Outline each blood parasite and name the species.
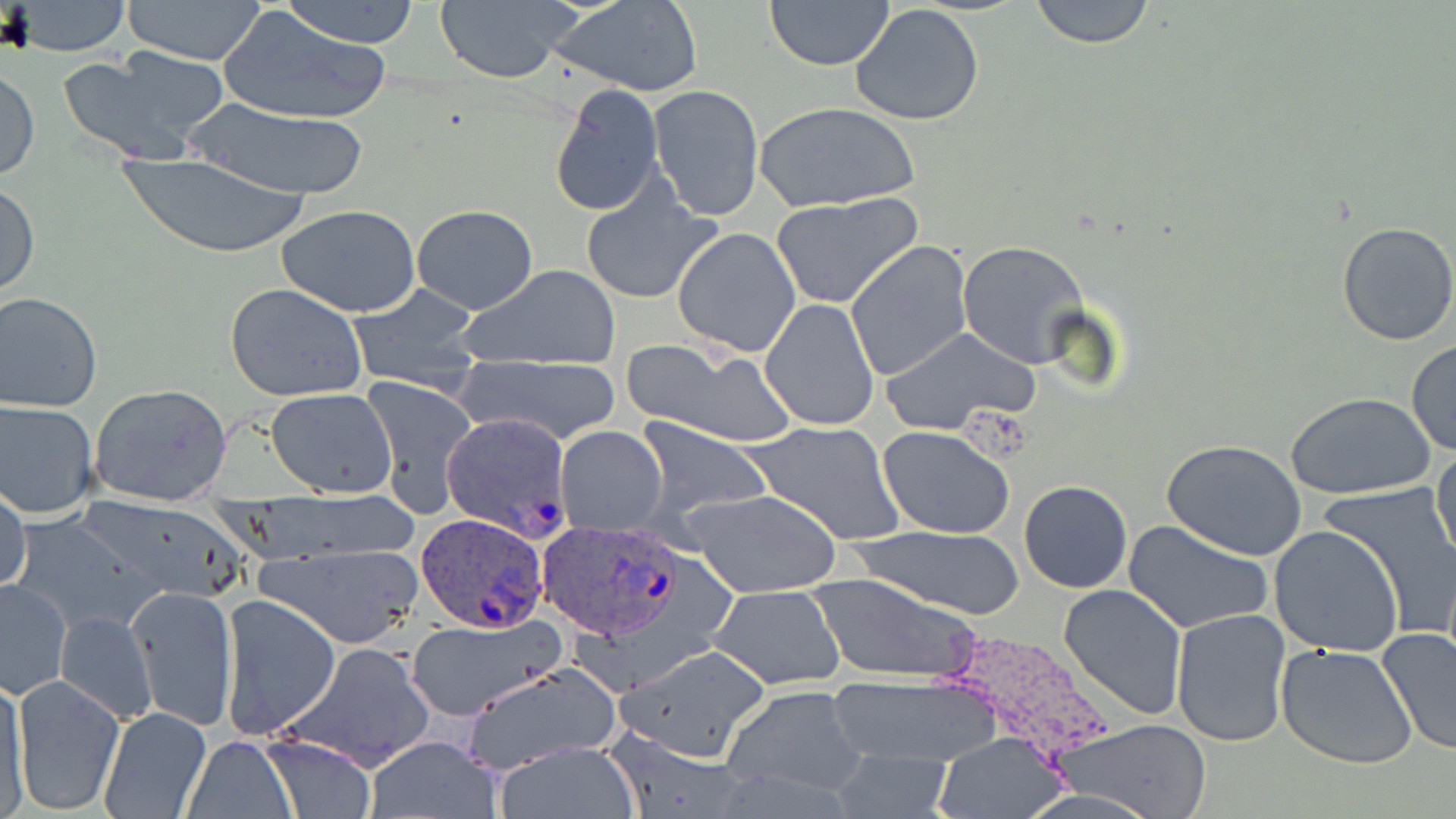
Approximate bounding boxes as (x1,y1)-(x2,y2) corner pairs in pixels.
Plasmodium ovale-infected red blood cells: (441,413)-(572,535), (415,513)-(551,635), (533,520)-(690,643).
No Plasmodium falciparum, Plasmodium malariae, Plasmodium vivax, Babesia divergens, or Trypanosoma brucei observed.

slide_level_diagnosis: Plasmodium ovale
image_size: 1456×819 pixels
magnification: 1000x
stain: May-Grünwald-Giemsa
modality: light microscopy
uninfected_red_blood_cell_locations: 'approximate bounding boxes as (x1,y1)-(x2,y2) corner pairs in pixels: (122,0)-(271,65), (279,0)-(423,47), (435,0)-(578,84), (765,0)-(896,72), (1029,0)-(1155,48), (9,1)-(132,55), (549,1)-(703,95), (850,4)-(987,128), (219,8)-(393,126), (57,51)-(222,165), (0,65)-(40,182), (549,83)-(665,217), (648,86)-(764,221), (180,99)-(375,200), (755,101)-(919,211), (112,152)-(318,258), (580,179)-(721,306), (0,180)-(39,300), (769,195)-(921,309), (276,204)-(422,317), (411,204)-(538,314), (1335,221)-(1456,346), (672,227)-(802,358), (843,239)-(972,382), (958,239)-(1090,368), (458,263)-(622,372), (225,282)-(368,402), (347,283)-(485,392), (0,291)-(103,413), (760,297)-(881,432), (880,327)-(1038,436), (1405,339)-(1456,456), (629,340)-(799,447), (457,353)-(622,446), (363,376)-(477,517), (89,384)-(233,505), (266,388)-(397,498), (1286,392)-(1436,501), (0,401)-(99,518), (634,419)-(769,525), (743,421)-(905,546), (879,425)-(1015,539), (556,427)-(669,532), (1162,439)-(1308,562), (1431,443)-(1456,571), (1019,480)-(1132,594), (1,482)-(29,596), (1320,483)-(1456,632), (683,486)-(841,599), (70,497)-(257,604), (15,511)-(156,639), (1123,520)-(1274,636), (849,522)-(1027,622), (1267,525)-(1405,659), (258,542)-(423,648), (806,572)-(983,683), (1,579)-(72,699), (708,584)-(846,689), (1058,584)-(1187,721), (127,585)-(237,730), (219,594)-(342,740), (1171,608)-(1292,747), (56,612)-(157,723), (407,618)-(559,718), (1375,627)-(1456,756), (1276,641)-(1420,770), (284,642)-(434,771), (619,645)-(768,760), (458,665)-(623,771), (2,674)-(30,815), (10,674)-(124,815), (828,676)-(1000,772), (720,685)-(870,802), (97,706)-(210,818), (1061,720)-(1214,816), (936,731)-(1063,817), (365,734)-(502,819), (259,735)-(379,817), (184,736)-(299,817), (495,741)-(640,816), (827,749)-(954,818)'
field_of_view: one of a larger specimen
preparation: thin blood smear